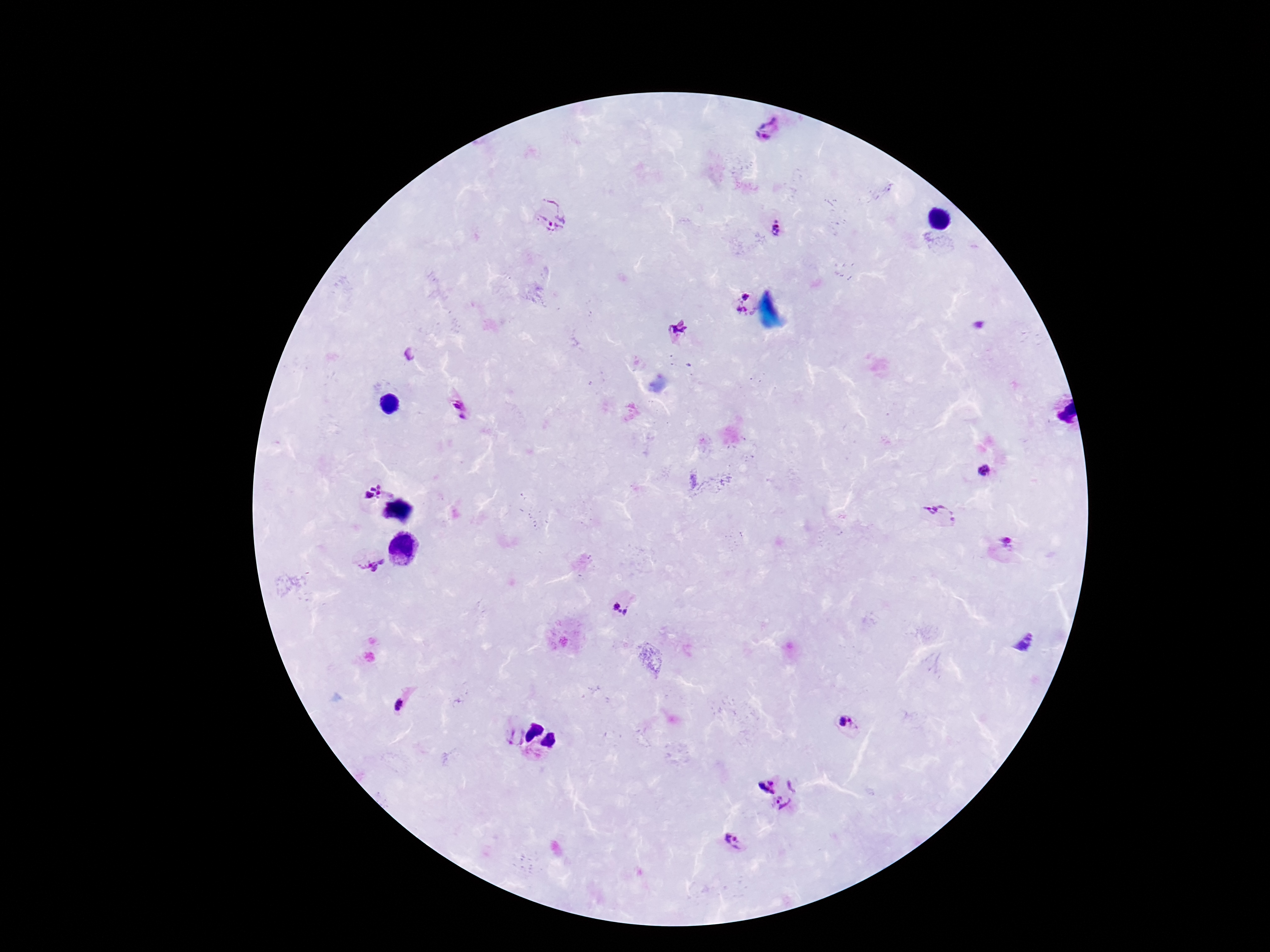

capture = smartphone camera through the microscope eyepiece
patient malaria status = infected
magnification = 100x
image size = 1270×952 pixels
Plasmodium parasite locations = approximate object centers, in pixels from the top-left corner: (x=769, y=128), (x=552, y=215), (x=775, y=228), (x=745, y=294), (x=744, y=313), (x=680, y=330), (x=408, y=355), (x=461, y=409), (x=984, y=470), (x=370, y=490), (x=940, y=514), (x=1008, y=542), (x=371, y=565), (x=619, y=609), (x=401, y=707), (x=842, y=721), (x=851, y=721), (x=514, y=734), (x=792, y=784), (x=767, y=787), (x=783, y=803), (x=733, y=841)
field of view = one from this slide
stain = Giemsa
preparation = thick peripheral-blood smear